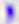
identification = Toxoplasma gondii
modality = micrograph
magnification = 400x